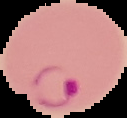
Summary:
  - Malaria status: parasitized
  - Preparation: thin blood smear
  - Image size: 127×118 pixels
  - Image type: segmented cell region on a black background